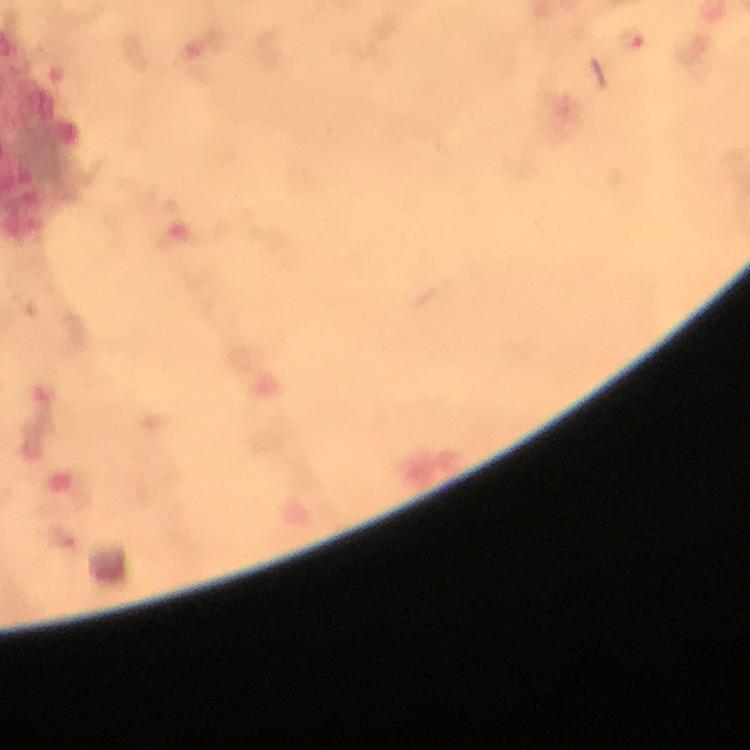

immersion oil = applied
stain = Giemsa
preparation = thick blood film
malaria parasite locations = approximate centers as [x, y] in pixels: [633, 41]
cropped from = one field of view
capture = smartphone photograph through a microscope
image size = 750×750 pixels
magnification = 100x
context = from a diagnostic examination for malaria